Outline each Plasmodium malariae-infected red blood cell.
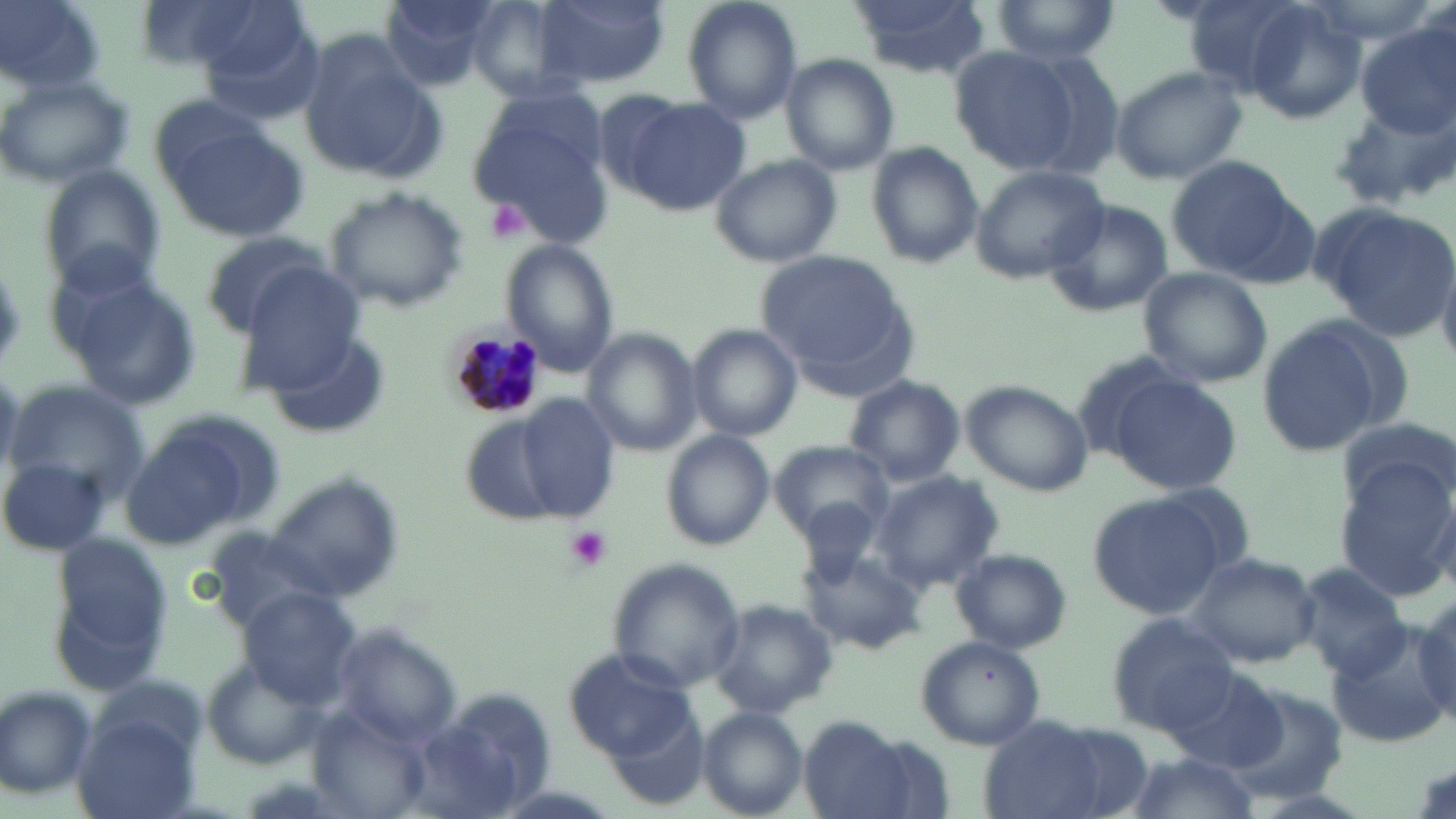

Approximate bounding boxes as (x1,y1)-(x2,y2) corner pairs in pixels.
Plasmodium malariae-infected red blood cells: (442,314)-(554,420).

Summary:
  - Uninfected red blood cell locations: (1,0)-(107,94), (139,0)-(294,74), (376,0)-(508,88), (536,0)-(667,88), (680,0)-(804,126), (845,0)-(993,77), (1175,0)-(1324,97), (464,1)-(580,101), (988,1)-(1121,64), (1238,2)-(1368,126), (181,3)-(320,108), (1354,24)-(1456,142), (296,34)-(443,181), (948,46)-(1080,172), (1011,47)-(1128,179), (782,55)-(899,175), (1107,65)-(1249,185), (0,74)-(134,185), (613,95)-(752,213), (1332,98)-(1456,209), (469,101)-(614,245), (157,115)-(306,241), (868,141)-(983,271), (1163,154)-(1305,280), (709,155)-(844,268), (40,166)-(167,295), (971,167)-(1108,282), (323,187)-(469,314), (1040,198)-(1174,317), (1313,201)-(1456,340), (198,231)-(334,338), (502,241)-(619,374), (758,251)-(907,369), (240,266)-(368,385), (1136,267)-(1273,388), (58,268)-(203,411), (1254,315)-(1404,459), (687,326)-(802,441), (581,329)-(700,456), (254,331)-(390,439), (843,373)-(965,488), (1106,374)-(1244,496), (3,377)-(149,506), (961,379)-(1093,496), (517,396)-(620,517), (127,410)-(285,546), (1337,414)-(1454,517), (462,420)-(565,525), (662,431)-(774,549), (771,440)-(897,544), (0,454)-(113,560), (1331,456)-(1456,598), (870,472)-(1003,591), (266,476)-(404,601), (1087,492)-(1229,618), (200,525)-(349,632), (44,528)-(176,694), (799,547)-(925,656), (951,549)-(1072,654), (1183,550)-(1321,667), (1296,559)-(1413,678), (607,560)-(746,694), (242,589)-(363,707), (1409,595)-(1456,731), (709,598)-(838,721), (1105,614)-(1240,741), (1326,623)-(1456,748), (326,624)-(463,749), (914,635)-(1046,750), (563,647)-(696,761), (204,660)-(324,769), (1166,668)-(1286,774), (411,684)-(559,818), (0,685)-(99,802), (1224,686)-(1348,805), (695,707)-(809,818), (310,711)-(435,819), (74,713)-(202,819), (976,716)-(1143,819), (799,717)-(924,819), (1116,753)-(1263,819)
  - Platelet locations: (491,200)-(530,237), (564,524)-(612,572)
  - Slide-level diagnosis: Plasmodium malariae
  - Modality: optical microscopy
  - Preparation: thin blood smear
  - Magnification: 1000x
  - Field of view: single
  - Stain: May-Grünwald-Giemsa
  - Image size: 1456×819 pixels